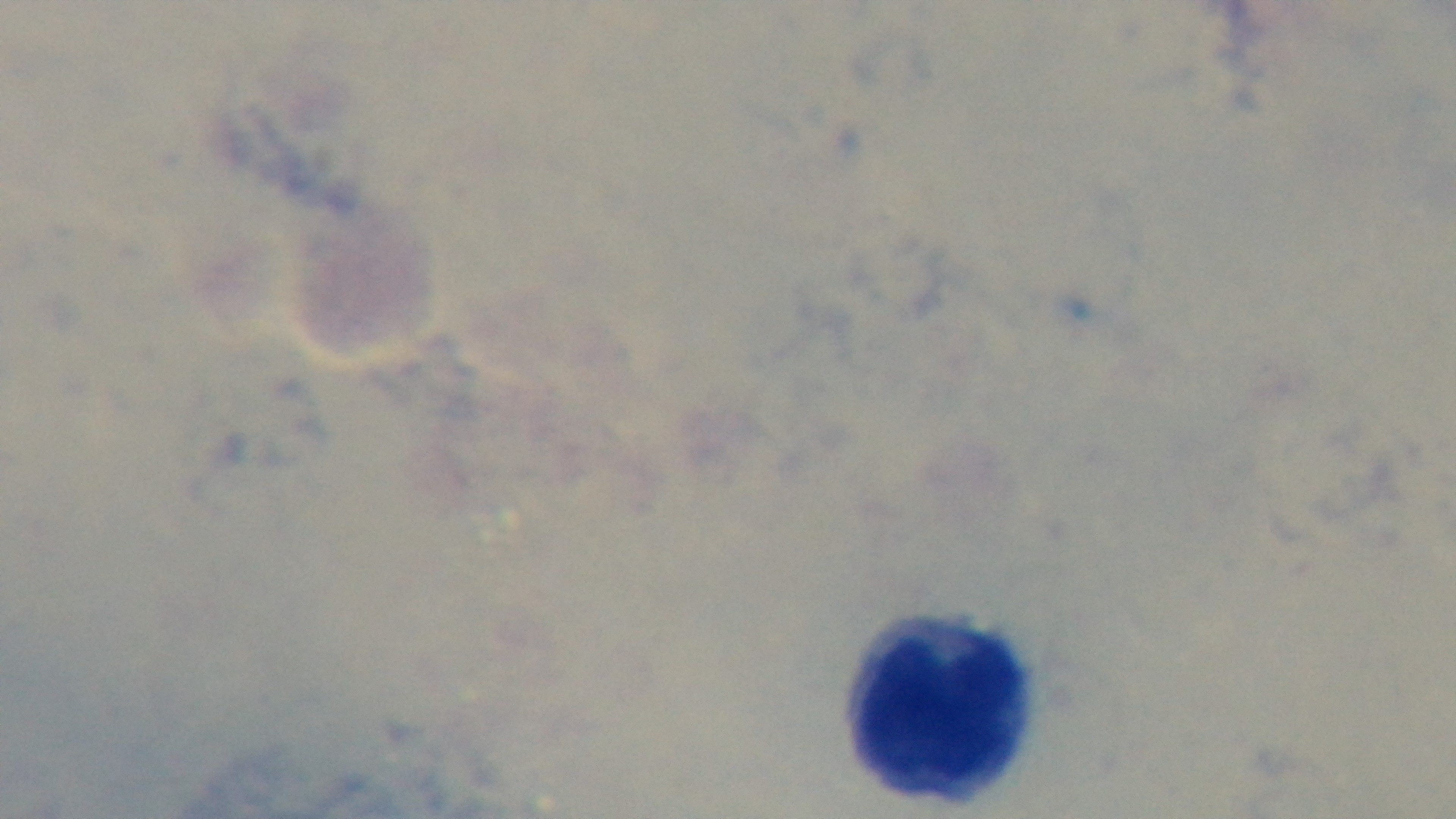 Single field of view. Giemsa-stained. Preparation: thick smear. Captured with a mounted 4K digital camera. Malaria status: negative. Light microscopy. 100x oil-immersion objective.